Classify this cell by malaria status.
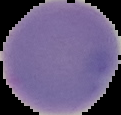

Uninfected.

Image is 121×115 pixels. From a thin blood film. The area outside the segmented cell region is set to black.